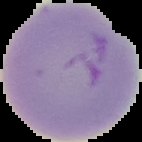

Segmented cell region on a black background. From a thin blood film. Malaria status: uninfected. Image is 142×142 pixels.